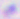

Summary:
  - Magnification: 400x
  - Modality: photomicrograph
  - Identification: Toxoplasma gondii